Classify this cell by malaria status.
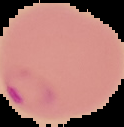

Parasitized.

From a thin blood smear. Image is 124×127 pixels. Cell region segmented out of the field of view; the surrounding area is masked to black.